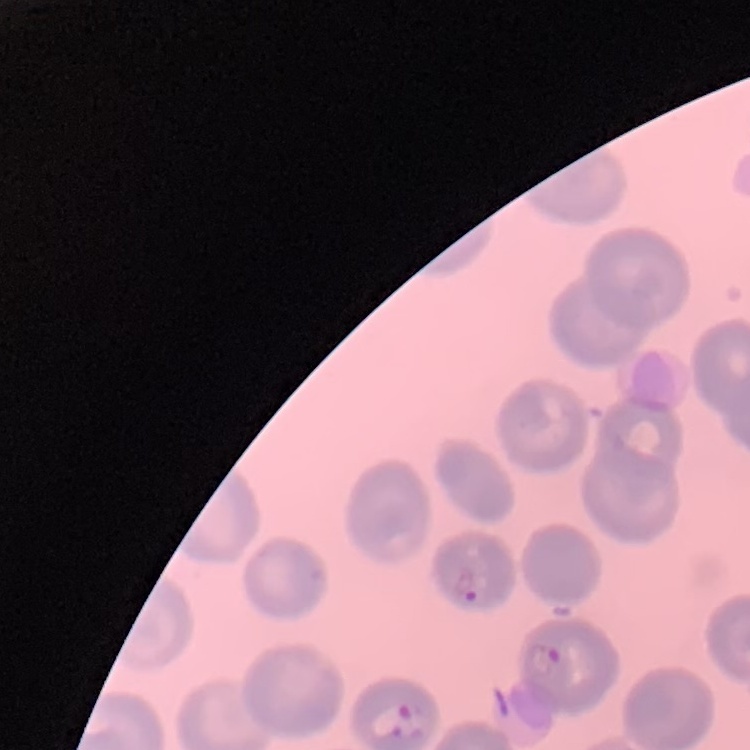

The erythrocytes exhibit no rouleaux formation. Thin blood film. One tile cut from a larger photomicrograph. Stained with either Field's or Giemsa.